Classify this cell by malaria status.
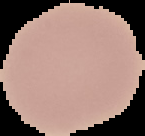
Uninfected.

From a thin blood film. Image is 145×136 pixels. The area outside the segmented cell region is set to black.